Identify the blood parasite species.
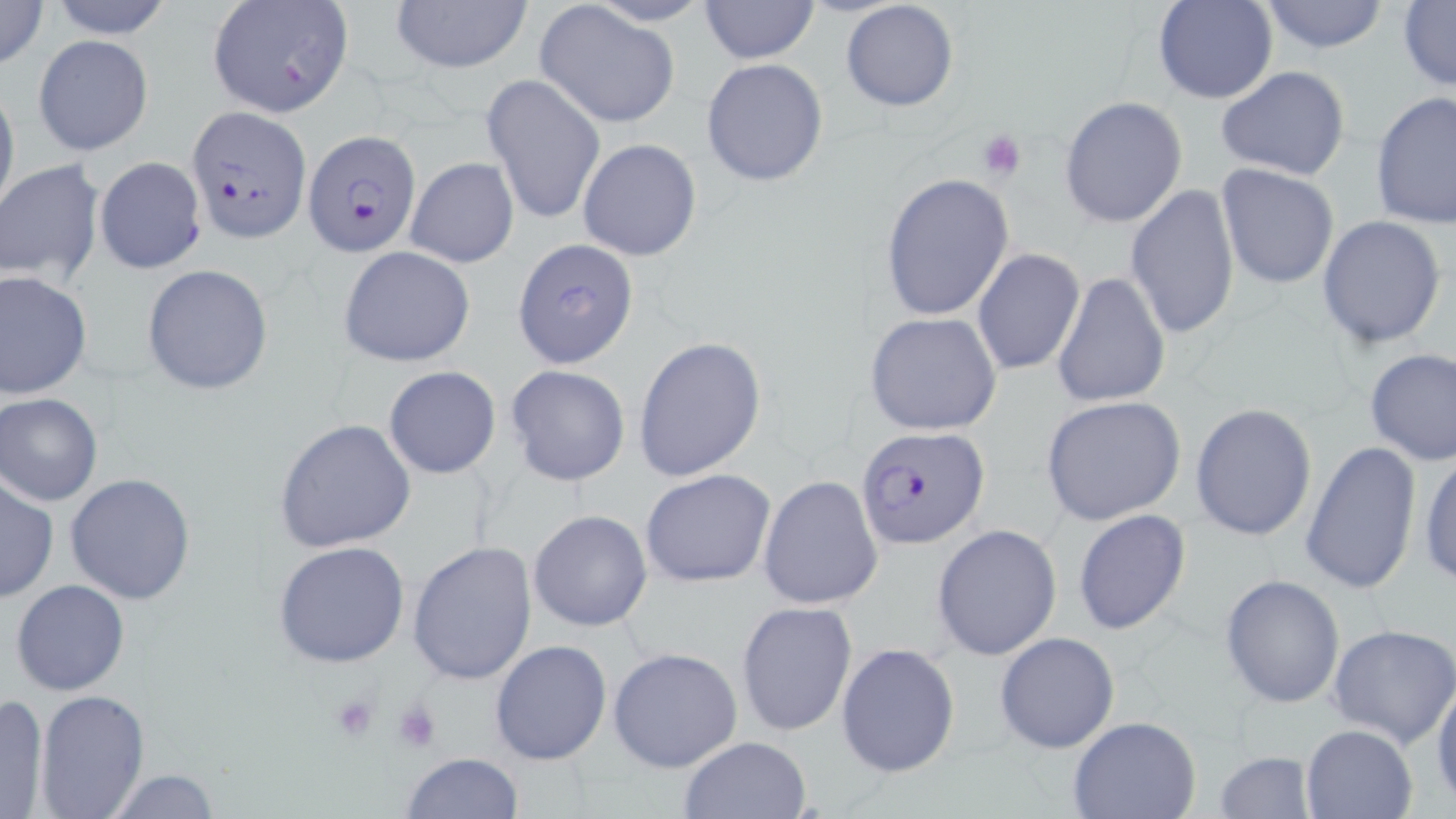
Plasmodium falciparum.

Summary:
  - Coordinate format: approximate bounding boxes as (x1,y1)-(x2,y2) corner pairs in pixels
  - Platelet locations: (977,127)-(1029,182), (327,693)-(382,742), (390,698)-(443,754)
  - Plasmodium falciparum-infected red blood cell locations: (184,104)-(309,242), (303,130)-(421,257), (856,427)-(990,549)
  - Uninfected red blood cell locations: (0,0)-(49,71), (44,0)-(177,39), (390,0)-(533,75), (697,0)-(820,64), (1153,0)-(1275,104), (1255,0)-(1392,54), (205,1)-(356,118), (840,1)-(959,113), (1397,1)-(1456,93), (533,4)-(679,127), (32,34)-(154,157), (701,58)-(827,187), (1214,66)-(1352,181), (482,72)-(605,226), (0,79)-(19,222), (1370,90)-(1454,232), (1059,96)-(1187,229), (578,137)-(702,261), (94,156)-(207,274), (405,156)-(520,269), (1,161)-(104,286), (1215,164)-(1340,290), (880,171)-(1015,323), (1125,182)-(1240,339), (1316,215)-(1447,350), (513,239)-(639,368), (338,245)-(476,368), (971,247)-(1086,376), (141,264)-(274,394), (1,271)-(93,398), (1052,271)-(1170,408), (866,311)-(1002,435), (633,336)-(766,482), (1363,348)-(1456,466), (506,364)-(631,487), (383,366)-(501,479), (0,393)-(103,505), (1041,396)-(1187,526), (1190,402)-(1317,543), (274,418)-(416,553), (1300,439)-(1422,596), (1417,448)-(1456,588), (642,468)-(776,588), (64,473)-(196,605), (760,475)-(885,611), (0,478)-(58,602), (1073,508)-(1191,636), (527,510)-(653,630), (931,524)-(1061,660), (407,540)-(538,686), (274,541)-(410,667), (1220,575)-(1343,707), (10,579)-(129,697), (735,602)-(857,736), (1327,624)-(1456,748), (994,631)-(1119,753), (488,638)-(612,767), (836,643)-(958,779), (608,646)-(744,773), (1431,672)-(1456,807), (34,690)-(151,819), (0,693)-(50,817), (1067,716)-(1202,819), (1300,723)-(1419,818), (678,735)-(812,818), (1215,748)-(1317,819), (398,751)-(524,818), (100,769)-(222,818)
  - Modality: optical microscopy
  - Image size: 1456×819 pixels
  - Magnification: 1000x
  - Preparation: thin blood film
  - Stain: May-Grünwald-Giemsa
  - Field of view: one of a larger specimen